Assess this cell for malaria.
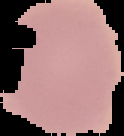

It is uninfected.

{
  "image_size": "124×136 pixels",
  "preparation": "thin blood smear",
  "image_type": "cell region segmented out of the field of view; surrounding area masked to black"
}